Give the extent of all Plasmodium ovale-infected red blood cells.
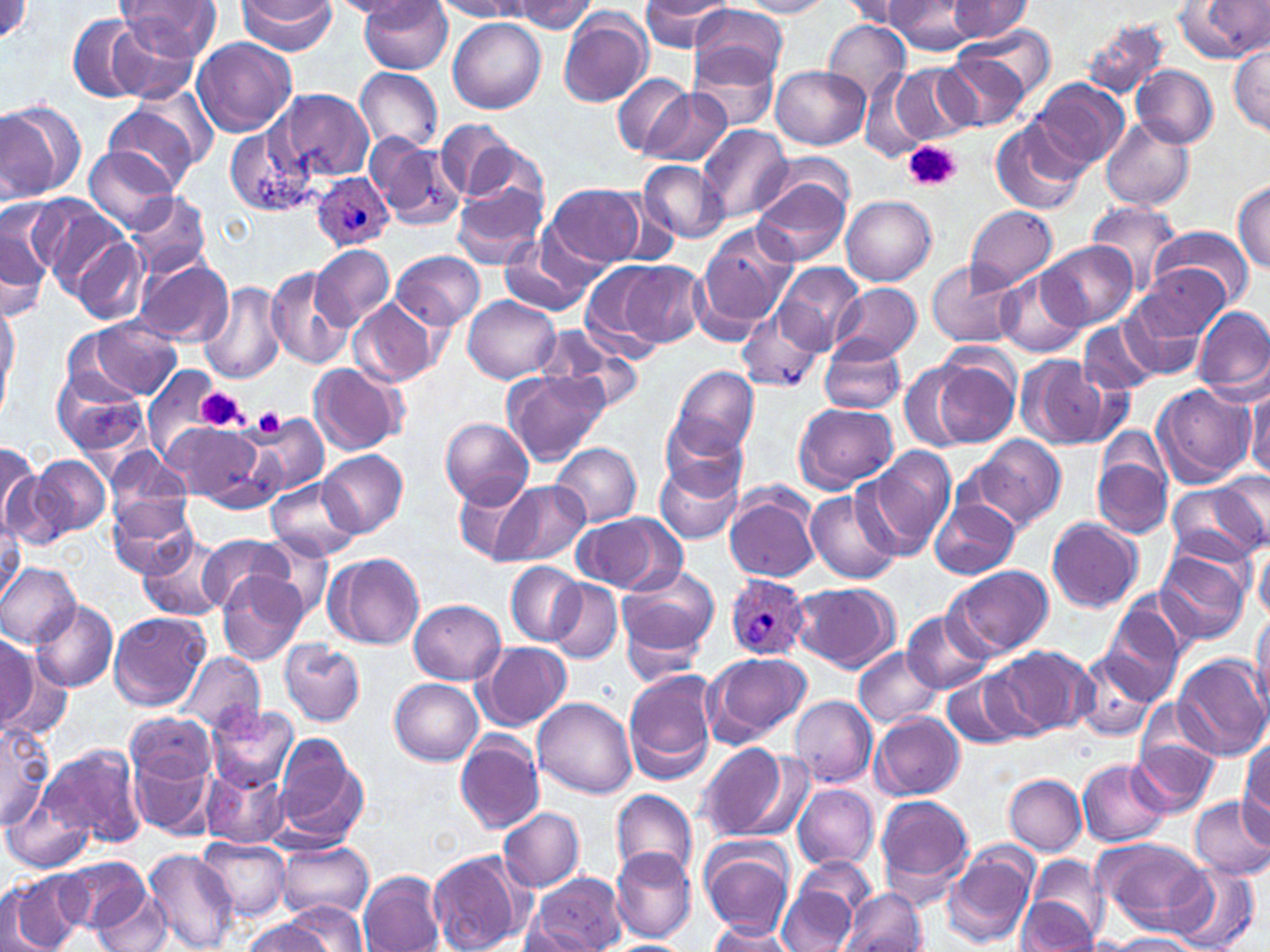
Approximate bounding boxes as named x1/y1/x2/y2 corners in pixels.
Plasmodium ovale-infected red blood cells: (x1=312, y1=173, x2=394, y2=251), (x1=725, y1=573, x2=810, y2=660).

Summary:
  - Uninfected red blood cell locations: (x1=0, y1=0, x2=32, y2=43), (x1=116, y1=0, x2=222, y2=63), (x1=735, y1=0, x2=835, y2=17), (x1=883, y1=0, x2=979, y2=55), (x1=236, y1=1, x2=334, y2=52), (x1=330, y1=1, x2=421, y2=17), (x1=436, y1=1, x2=531, y2=20), (x1=509, y1=1, x2=597, y2=34), (x1=840, y1=1, x2=916, y2=26), (x1=946, y1=1, x2=1033, y2=42), (x1=1178, y1=1, x2=1268, y2=62), (x1=359, y1=2, x2=453, y2=75), (x1=639, y1=2, x2=736, y2=52), (x1=689, y1=6, x2=788, y2=83), (x1=557, y1=8, x2=654, y2=108), (x1=68, y1=12, x2=154, y2=102), (x1=449, y1=18, x2=546, y2=114), (x1=106, y1=19, x2=200, y2=103), (x1=1080, y1=19, x2=1171, y2=101), (x1=821, y1=20, x2=911, y2=104), (x1=960, y1=28, x2=1055, y2=101), (x1=191, y1=37, x2=298, y2=137), (x1=1229, y1=44, x2=1270, y2=135), (x1=692, y1=49, x2=780, y2=131), (x1=936, y1=51, x2=1029, y2=132), (x1=771, y1=63, x2=870, y2=149), (x1=1132, y1=64, x2=1218, y2=148), (x1=890, y1=65, x2=973, y2=146), (x1=356, y1=68, x2=442, y2=154), (x1=861, y1=73, x2=931, y2=163), (x1=611, y1=74, x2=694, y2=158), (x1=1033, y1=78, x2=1130, y2=168), (x1=277, y1=88, x2=376, y2=179), (x1=639, y1=89, x2=734, y2=168), (x1=0, y1=98, x2=85, y2=201), (x1=101, y1=102, x2=202, y2=194), (x1=989, y1=116, x2=1087, y2=216), (x1=1099, y1=119, x2=1196, y2=212), (x1=224, y1=123, x2=318, y2=219), (x1=699, y1=125, x2=793, y2=223), (x1=442, y1=126, x2=544, y2=211), (x1=369, y1=137, x2=465, y2=231), (x1=84, y1=148, x2=175, y2=231), (x1=764, y1=153, x2=858, y2=221), (x1=638, y1=161, x2=729, y2=243), (x1=752, y1=179, x2=849, y2=268), (x1=1232, y1=180, x2=1270, y2=272), (x1=450, y1=181, x2=548, y2=269), (x1=547, y1=185, x2=646, y2=268), (x1=124, y1=190, x2=211, y2=279), (x1=842, y1=195, x2=937, y2=286), (x1=17, y1=196, x2=126, y2=290), (x1=1086, y1=201, x2=1182, y2=294), (x1=965, y1=204, x2=1057, y2=292), (x1=0, y1=215, x2=52, y2=318), (x1=1150, y1=224, x2=1255, y2=308), (x1=697, y1=225, x2=797, y2=330), (x1=73, y1=236, x2=149, y2=325), (x1=501, y1=236, x2=597, y2=316), (x1=1041, y1=242, x2=1138, y2=329), (x1=311, y1=244, x2=394, y2=330), (x1=391, y1=251, x2=485, y2=331), (x1=134, y1=256, x2=234, y2=348), (x1=364, y1=259, x2=475, y2=369), (x1=581, y1=261, x2=672, y2=353), (x1=927, y1=261, x2=1020, y2=348), (x1=620, y1=262, x2=708, y2=349), (x1=776, y1=263, x2=863, y2=352), (x1=265, y1=266, x2=351, y2=371), (x1=1133, y1=266, x2=1231, y2=355), (x1=995, y1=271, x2=1086, y2=356), (x1=199, y1=280, x2=285, y2=386), (x1=830, y1=283, x2=922, y2=362), (x1=464, y1=296, x2=561, y2=383), (x1=0, y1=298, x2=19, y2=411), (x1=348, y1=299, x2=439, y2=387), (x1=1125, y1=299, x2=1210, y2=378), (x1=737, y1=307, x2=824, y2=393), (x1=1195, y1=308, x2=1269, y2=395), (x1=79, y1=318, x2=182, y2=401), (x1=1080, y1=319, x2=1158, y2=397), (x1=537, y1=326, x2=646, y2=412), (x1=819, y1=337, x2=908, y2=416), (x1=1014, y1=352, x2=1115, y2=449), (x1=927, y1=357, x2=1016, y2=447), (x1=900, y1=360, x2=979, y2=453), (x1=309, y1=363, x2=404, y2=454), (x1=670, y1=366, x2=760, y2=460), (x1=52, y1=368, x2=148, y2=458), (x1=142, y1=368, x2=217, y2=461), (x1=503, y1=370, x2=608, y2=466), (x1=1151, y1=382, x2=1256, y2=489), (x1=1246, y1=389, x2=1269, y2=480), (x1=793, y1=401, x2=899, y2=492), (x1=245, y1=412, x2=329, y2=499), (x1=439, y1=416, x2=533, y2=506), (x1=660, y1=416, x2=749, y2=498), (x1=168, y1=421, x2=265, y2=505), (x1=970, y1=435, x2=1065, y2=530), (x1=550, y1=443, x2=642, y2=526), (x1=860, y1=446, x2=956, y2=558), (x1=1091, y1=447, x2=1173, y2=540), (x1=105, y1=450, x2=194, y2=537), (x1=319, y1=450, x2=407, y2=537), (x1=0, y1=451, x2=49, y2=542), (x1=31, y1=454, x2=110, y2=538), (x1=654, y1=459, x2=745, y2=544), (x1=455, y1=476, x2=540, y2=564), (x1=267, y1=477, x2=359, y2=563), (x1=1165, y1=479, x2=1269, y2=568), (x1=493, y1=480, x2=589, y2=565), (x1=724, y1=483, x2=822, y2=584), (x1=805, y1=490, x2=901, y2=585), (x1=929, y1=497, x2=1020, y2=580), (x1=109, y1=500, x2=196, y2=578), (x1=572, y1=512, x2=684, y2=594), (x1=1046, y1=518, x2=1143, y2=612), (x1=0, y1=520, x2=23, y2=598), (x1=250, y1=534, x2=336, y2=624), (x1=139, y1=535, x2=229, y2=621), (x1=196, y1=536, x2=294, y2=613), (x1=1254, y1=543, x2=1270, y2=619), (x1=1154, y1=548, x2=1253, y2=644), (x1=325, y1=552, x2=425, y2=650), (x1=505, y1=562, x2=586, y2=644), (x1=0, y1=563, x2=80, y2=648), (x1=616, y1=564, x2=720, y2=667), (x1=945, y1=565, x2=1055, y2=659), (x1=217, y1=569, x2=307, y2=666), (x1=931, y1=573, x2=1050, y2=733), (x1=547, y1=579, x2=622, y2=664), (x1=791, y1=582, x2=899, y2=672), (x1=408, y1=598, x2=506, y2=684), (x1=28, y1=599, x2=118, y2=692), (x1=1100, y1=603, x2=1186, y2=706), (x1=1250, y1=604, x2=1270, y2=717), (x1=108, y1=610, x2=210, y2=710), (x1=902, y1=611, x2=993, y2=694), (x1=0, y1=637, x2=56, y2=740), (x1=279, y1=640, x2=365, y2=726), (x1=478, y1=641, x2=572, y2=729), (x1=987, y1=645, x2=1094, y2=738), (x1=856, y1=647, x2=942, y2=730), (x1=701, y1=650, x2=813, y2=747), (x1=1072, y1=650, x2=1162, y2=740), (x1=177, y1=651, x2=264, y2=735), (x1=1171, y1=654, x2=1267, y2=760), (x1=623, y1=669, x2=720, y2=784), (x1=944, y1=671, x2=1027, y2=751), (x1=390, y1=679, x2=483, y2=765), (x1=790, y1=695, x2=878, y2=786), (x1=533, y1=697, x2=637, y2=798), (x1=208, y1=704, x2=299, y2=790), (x1=125, y1=711, x2=215, y2=786), (x1=871, y1=712, x2=964, y2=799), (x1=0, y1=719, x2=52, y2=830), (x1=1130, y1=722, x2=1223, y2=819), (x1=272, y1=734, x2=369, y2=845), (x1=455, y1=735, x2=545, y2=832), (x1=1238, y1=738, x2=1269, y2=836), (x1=37, y1=741, x2=146, y2=849), (x1=695, y1=742, x2=798, y2=843), (x1=129, y1=752, x2=217, y2=840), (x1=1078, y1=758, x2=1170, y2=846), (x1=202, y1=764, x2=289, y2=848), (x1=1003, y1=774, x2=1086, y2=855), (x1=792, y1=784, x2=877, y2=870), (x1=611, y1=789, x2=698, y2=883), (x1=875, y1=794, x2=975, y2=896), (x1=1188, y1=795, x2=1270, y2=880), (x1=3, y1=796, x2=94, y2=874), (x1=499, y1=807, x2=585, y2=892), (x1=698, y1=835, x2=797, y2=938), (x1=197, y1=837, x2=290, y2=921), (x1=1090, y1=837, x2=1215, y2=936), (x1=275, y1=838, x2=375, y2=923), (x1=943, y1=843, x2=1039, y2=951), (x1=612, y1=846, x2=698, y2=943), (x1=144, y1=849, x2=239, y2=952), (x1=426, y1=849, x2=529, y2=952), (x1=1025, y1=854, x2=1109, y2=946), (x1=55, y1=855, x2=145, y2=934), (x1=778, y1=858, x2=876, y2=952), (x1=1168, y1=863, x2=1261, y2=952), (x1=360, y1=869, x2=446, y2=952), (x1=4, y1=871, x2=86, y2=952), (x1=526, y1=872, x2=626, y2=952), (x1=842, y1=887, x2=926, y2=952), (x1=92, y1=890, x2=175, y2=952), (x1=1015, y1=896, x2=1096, y2=950), (x1=276, y1=902, x2=370, y2=950), (x1=242, y1=915, x2=335, y2=952), (x1=520, y1=925, x2=601, y2=950), (x1=706, y1=925, x2=798, y2=952), (x1=1101, y1=933, x2=1205, y2=951), (x1=601, y1=940, x2=698, y2=952)
  - Platelet locations: (x1=903, y1=141, x2=960, y2=192), (x1=194, y1=389, x2=247, y2=431), (x1=251, y1=407, x2=286, y2=440)
  - Slide-level diagnosis: Plasmodium ovale
  - Field of view: single
  - Stain: May-Grünwald-Giemsa
  - Image size: 1270×952 pixels
  - Modality: light microscopy
  - Magnification: 1000x
  - Preparation: thin blood film